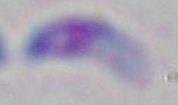

Micrograph. Toxoplasma gondii is seen. 1000x magnification.